State which parasite is depicted.
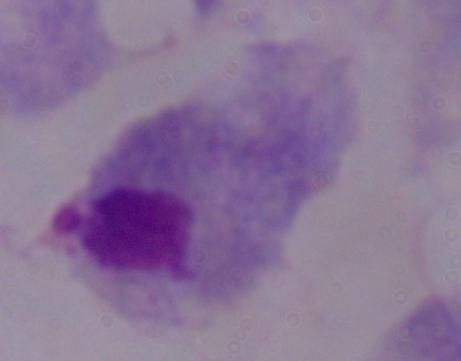

A trichomonad.

Micrograph. 1000x magnification.